Assess this cell for malaria.
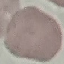

Uninfected.

stain = Giemsa
image type = automatically extracted cell patch, resized to 64 × 64 pixels
capture = smartphone camera at the microscope eyepiece
preparation = thin smear